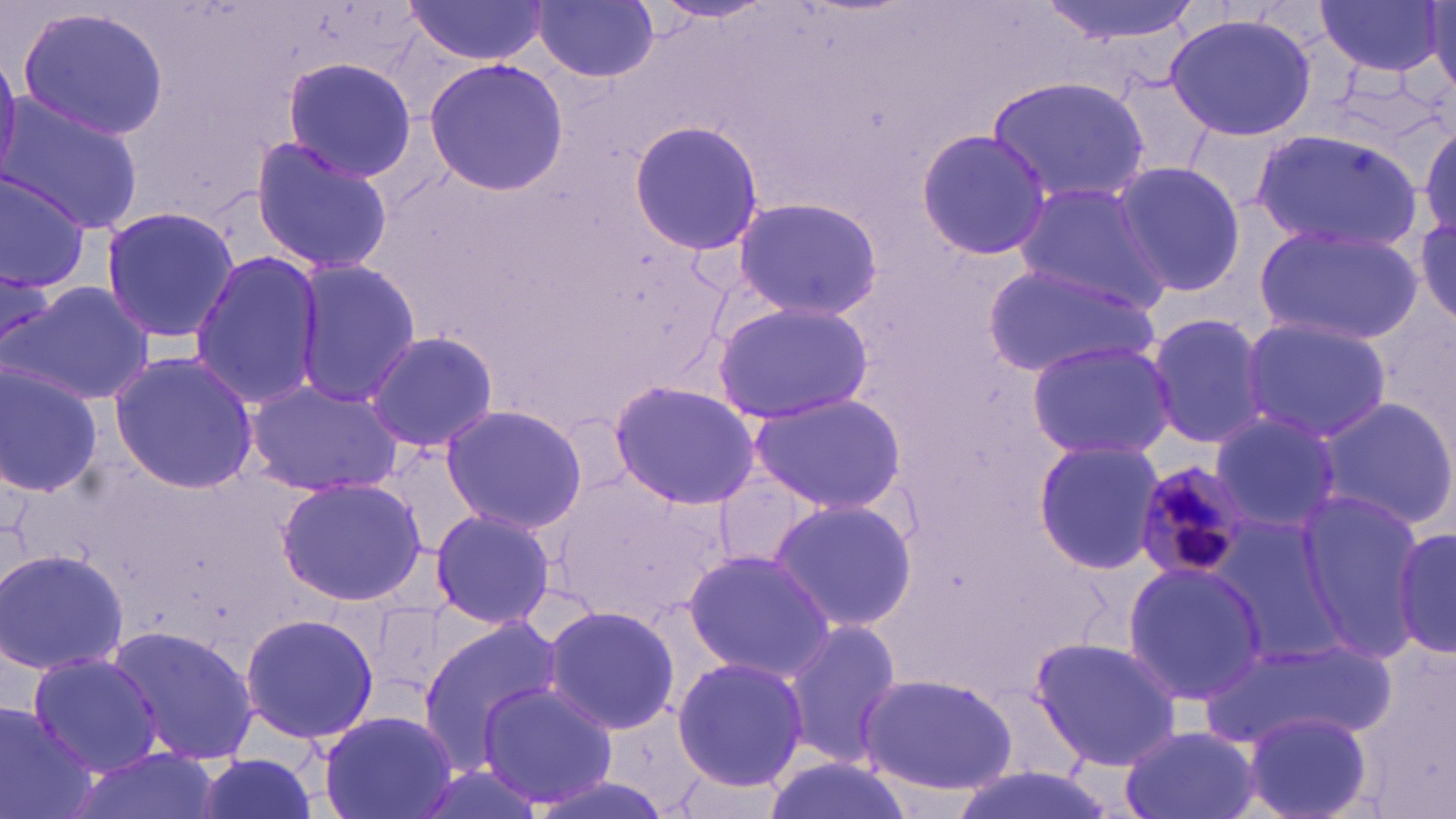

{
  "plasmodium_malariae_infected_red_blood_cell_locations": "approximate bounding boxes as (x1,y1)-(x2,y2) corner pairs in pixels: (1132,463)-(1249,583)",
  "slide_level_diagnosis": "Plasmodium malariae",
  "uninfected_red_blood_cell_locations": "approximate bounding boxes as (x1,y1)-(x2,y2) corner pairs in pixels: (653,0)-(775,24), (1036,0)-(1204,51), (1314,0)-(1449,78), (534,1)-(661,83), (403,2)-(549,65), (1429,3)-(1456,95), (13,6)-(171,140), (1163,11)-(1322,139), (281,57)-(417,182), (424,58)-(567,195), (987,76)-(1153,206), (2,94)-(147,235), (1420,120)-(1455,239), (629,121)-(766,253), (915,130)-(1053,260), (1252,130)-(1425,253), (250,135)-(394,275), (1111,158)-(1245,297), (0,170)-(93,294), (1013,180)-(1170,310), (730,195)-(884,319), (98,204)-(240,346), (1415,216)-(1454,325), (1253,221)-(1421,346), (186,251)-(323,412), (290,259)-(420,406), (984,262)-(1161,378), (9,279)-(155,408), (711,298)-(872,425), (1144,311)-(1272,451), (1239,316)-(1397,444), (364,330)-(500,452), (1024,339)-(1177,460), (108,351)-(260,495), (0,361)-(103,498), (244,379)-(408,497), (606,380)-(761,509), (746,394)-(907,513), (1317,396)-(1456,531), (439,405)-(589,534), (1208,408)-(1344,533), (1032,441)-(1167,575), (714,473)-(821,572), (274,478)-(429,606), (1291,491)-(1431,660), (768,497)-(919,633), (429,507)-(556,631), (1210,514)-(1351,662), (1393,524)-(1455,660), (0,548)-(129,678), (681,548)-(837,682), (1121,559)-(1268,708), (542,605)-(681,736), (238,610)-(379,747), (414,611)-(562,775), (776,619)-(903,771), (109,627)-(262,765), (1028,634)-(1183,770), (1199,635)-(1398,751), (23,648)-(163,779), (670,656)-(810,793), (857,672)-(1020,795), (478,680)-(620,809), (0,705)-(94,819), (317,706)-(459,819), (1241,710)-(1373,819), (1118,725)-(1262,819), (62,745)-(224,819), (192,754)-(321,819), (761,756)-(915,819), (943,767)-(1123,819)",
  "magnification": "1000x",
  "image_size": "1456×819 pixels",
  "field_of_view": "one of a larger specimen",
  "stain": "May-Grünwald-Giemsa",
  "modality": "optical microscopy",
  "preparation": "thin blood film"
}